Classify this cell by malaria status.
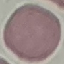
Uninfected.

Summary:
  - Capture: smartphone camera at the microscope eyepiece
  - Image type: cell patch, automatically extracted from a larger field of view and resized to 64 × 64 pixels
  - Preparation: thin smear
  - Stain: Giemsa